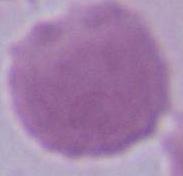

Summary:
  - Magnification: 1000x
  - Identification: erythrocyte
  - Modality: micrograph